Outline each uninfected red blood cell.
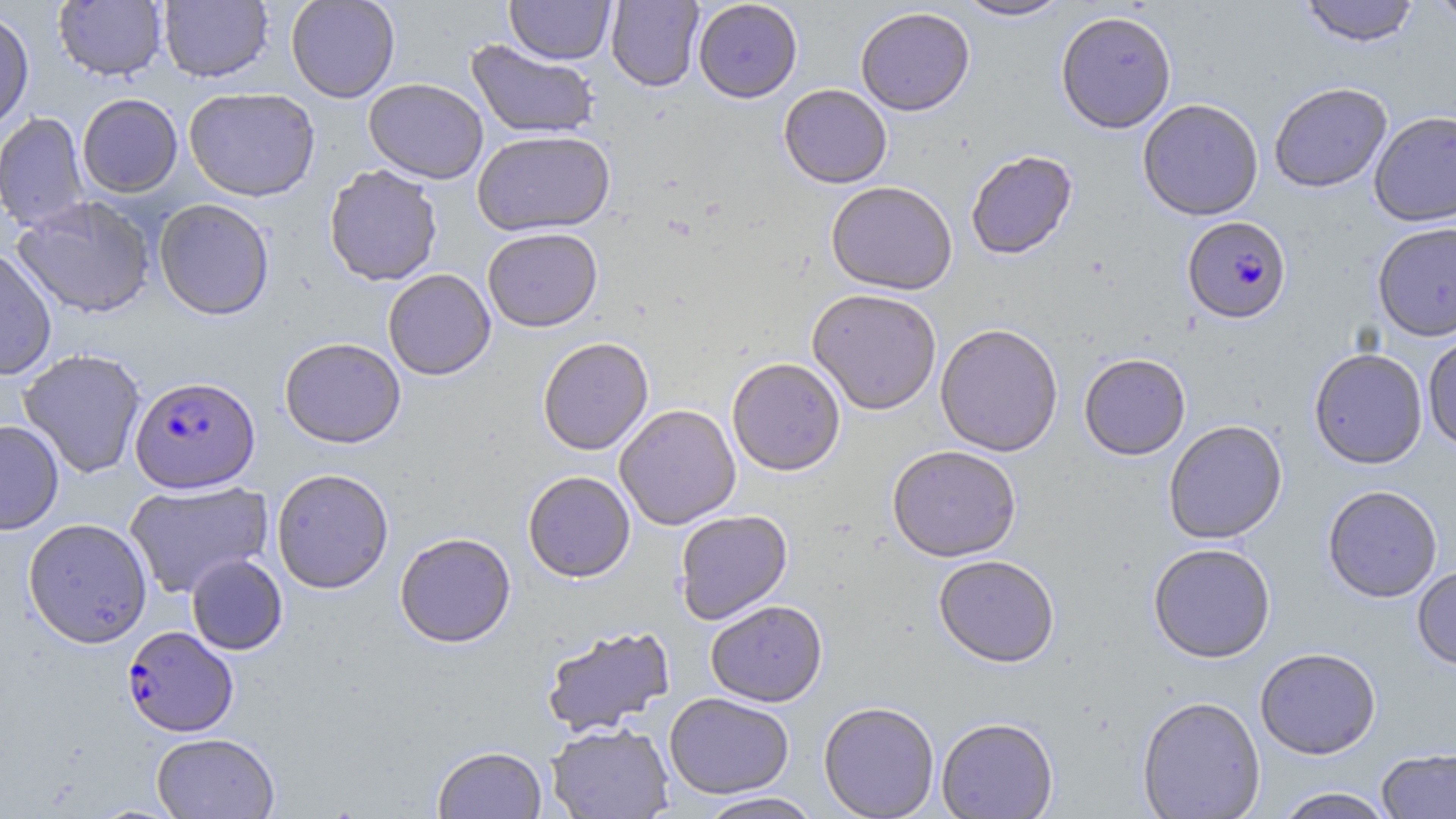

Approximate bounding boxes as (x1,y1)-(x2,y2) corner pairs in pixels.
Uninfected red blood cells: (53,0)-(167,82), (158,0)-(273,83), (286,0)-(400,103), (505,0)-(615,64), (606,0)-(704,92), (693,0)-(803,103), (954,0)-(1070,21), (1299,0)-(1420,47), (1424,0)-(1456,25), (0,6)-(35,133), (855,6)-(975,115), (1056,10)-(1177,133), (465,39)-(600,140), (363,78)-(488,184), (1269,82)-(1392,193), (778,84)-(892,188), (184,87)-(321,201), (77,93)-(183,197), (1137,98)-(1264,221), (1369,110)-(1456,227), (0,112)-(90,232), (472,130)-(615,236), (965,150)-(1078,261), (323,165)-(442,286), (826,181)-(957,295), (12,196)-(156,319), (154,198)-(275,321), (1372,222)-(1456,341), (482,227)-(603,332), (0,247)-(58,381), (383,268)-(496,380), (807,288)-(942,415), (935,322)-(1063,457), (1422,331)-(1456,454), (279,337)-(406,449), (537,337)-(654,456), (17,348)-(146,478), (1309,348)-(1428,469), (1079,353)-(1191,460), (727,357)-(846,475), (615,403)-(741,530), (0,419)-(64,535), (1163,420)-(1288,544), (886,445)-(1022,562), (271,467)-(394,594), (522,470)-(635,582), (124,479)-(273,598), (1322,485)-(1442,603), (674,509)-(792,624), (23,517)-(152,648), (394,532)-(516,648), (1148,543)-(1276,663), (186,554)-(288,655), (933,554)-(1060,668), (1412,565)-(1456,670), (705,599)-(828,707), (541,624)-(675,737), (1255,647)-(1382,760), (664,692)-(794,799), (1137,696)-(1265,818), (818,701)-(939,818), (936,717)-(1058,818), (545,722)-(674,818), (151,732)-(279,819), (432,745)-(547,818), (1377,748)-(1456,818), (1273,787)-(1395,818), (695,792)-(825,819).

Plasmodium falciparum-infected red blood cell locations: (1183,217)-(1291,324), (130,375)-(260,493), (122,626)-(238,737). Slide-level diagnosis: Plasmodium falciparum. May-Grünwald-Giemsa-stained preparation. Image is 1456×819 pixels. 1000x magnification. Light microscopy. One field of a larger specimen. Thin blood film.